Name the parasite shown.
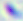
This is Toxoplasma gondii.

Summary:
  - Magnification: 400x
  - Modality: micrograph